Report the malaria status.
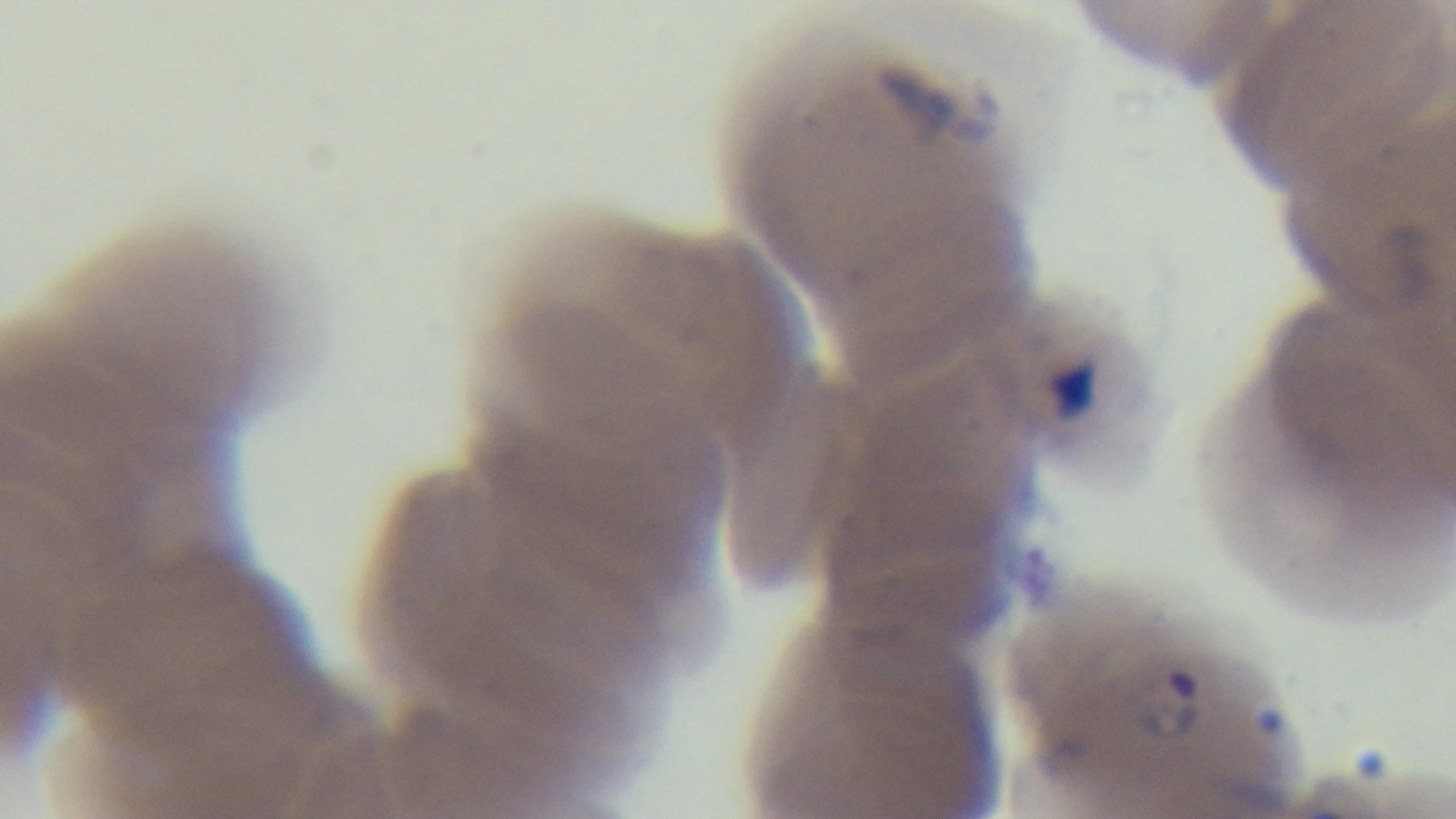

Positive.

Summary:
  - Stain: Giemsa
  - Preparation: thin blood film
  - Capture: mounted 4K digital camera
  - Modality: light microscopy
  - Field of view: single
  - Objective: 100x oil immersion